Give the preparation type.
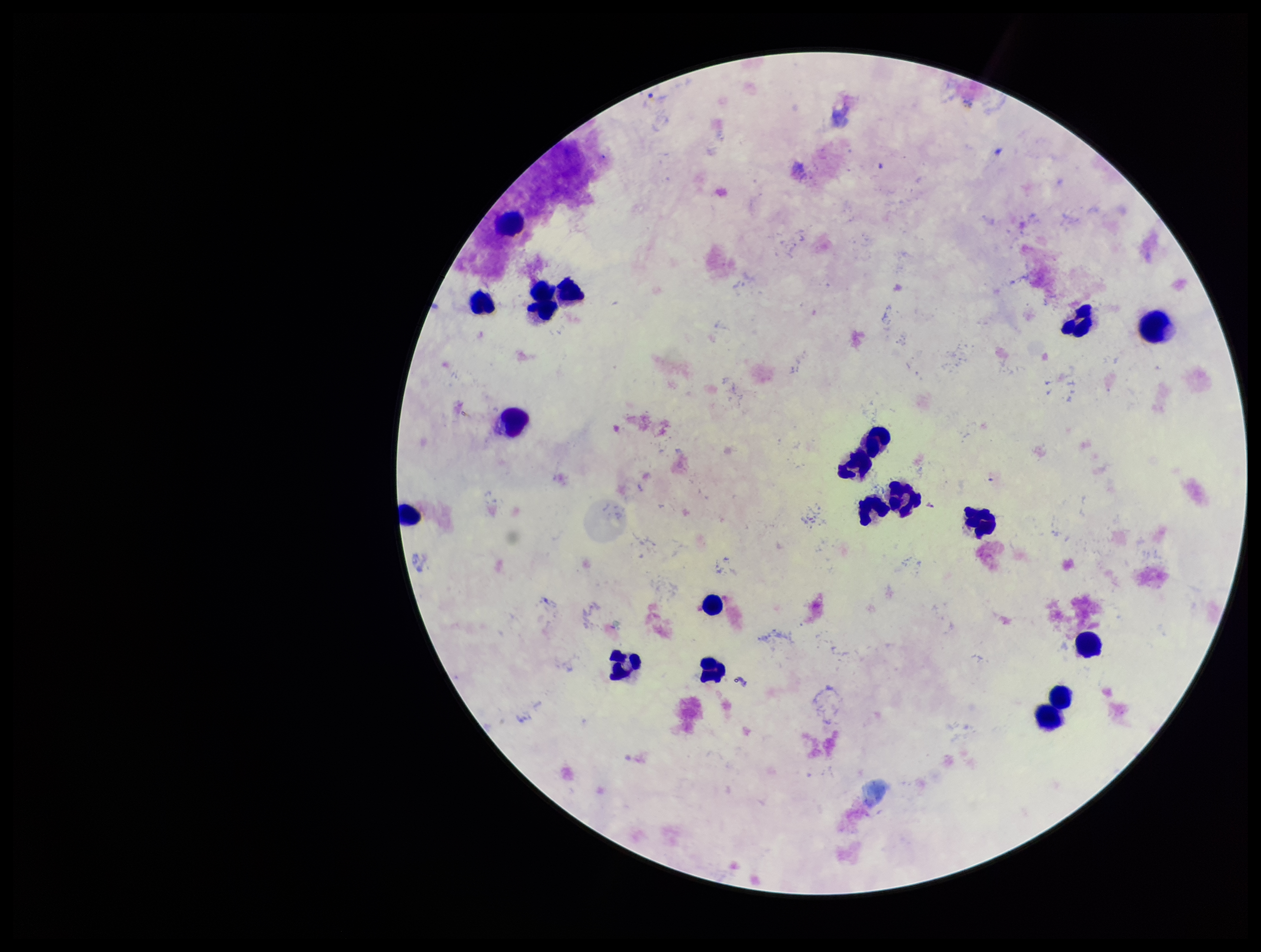
It is a thick blood smear.

patient malaria status = infected
stain = Giemsa
leukocyte count = 19
field of view = one from this slide
image size = 1261×952 pixels
capture = smartphone photograph through the microscope eyepiece
Plasmodium parasites = none seen
species reported for this patient = Plasmodium vivax
parasite count = 0